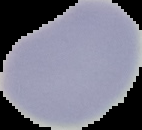
result = no Plasmodium parasites seen
preparation = thin blood film
image size = 142×130 pixels
image type = segmented cell region on a black background